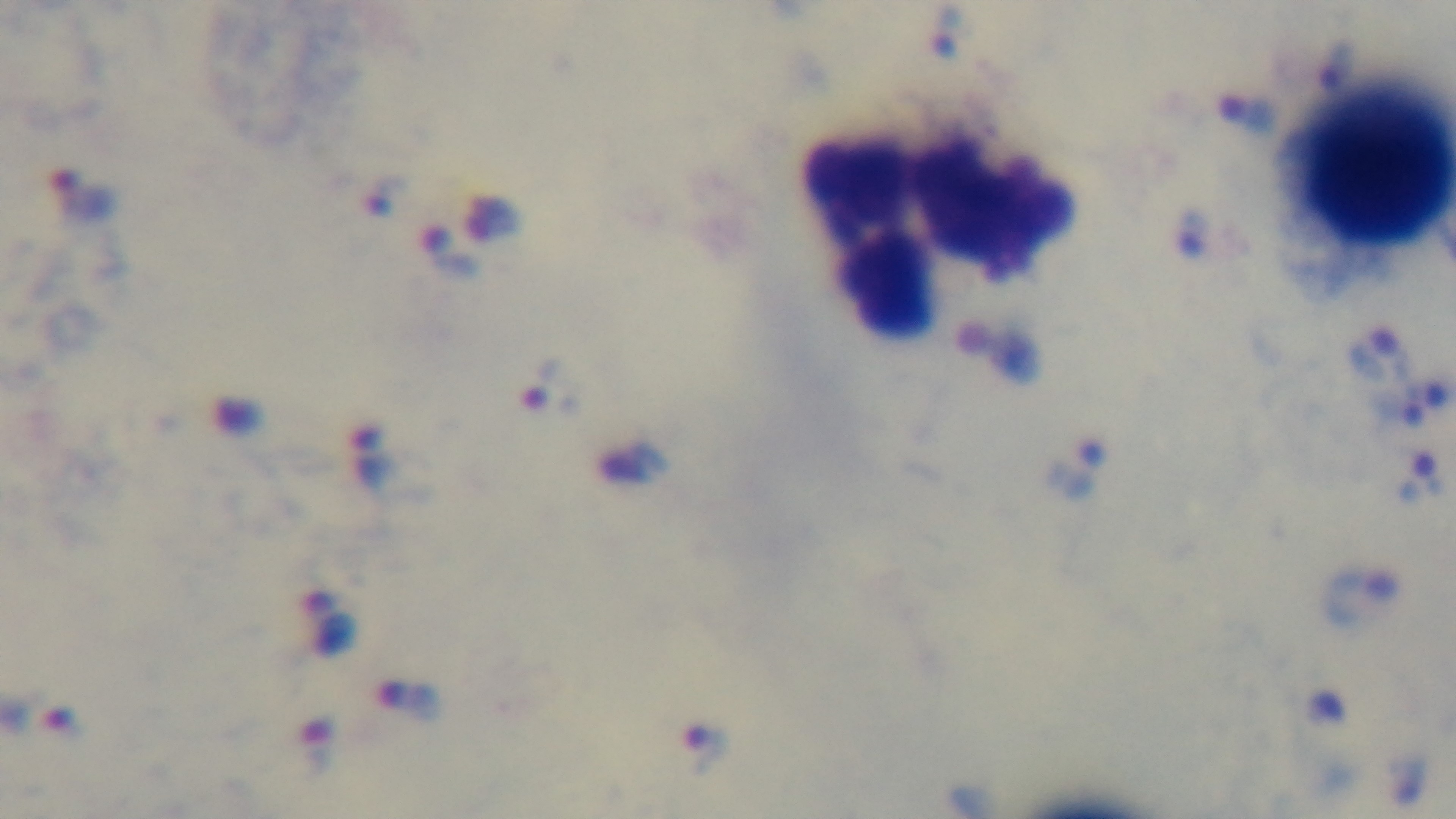
Summary:
  - Malaria status: positive
  - Objective: 100x oil immersion
  - Field of view: one from the slide
  - Stain: Giemsa
  - Modality: light microscopy
  - Preparation: thick
  - Capture: mounted 4K digital camera